Identify the parasite.
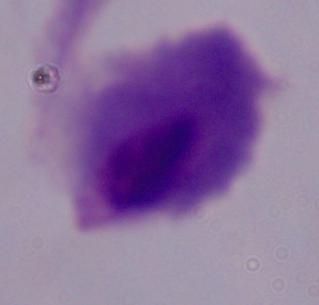

This is a trichomonad.

{
  "magnification": "1000x",
  "modality": "photomicrograph"
}